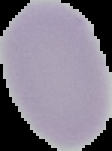 From a thin blood smear. Cell region segmented out of the field of view; the surrounding area is masked to black. Malaria status: uninfected. Image is 112×151 pixels.